Classify this cell by malaria status.
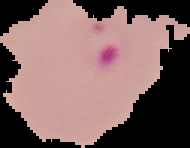

Parasitized.

Summary:
  - Preparation: thin blood smear
  - Image size: 190×148 pixels
  - Image type: segmented cell region on a black background